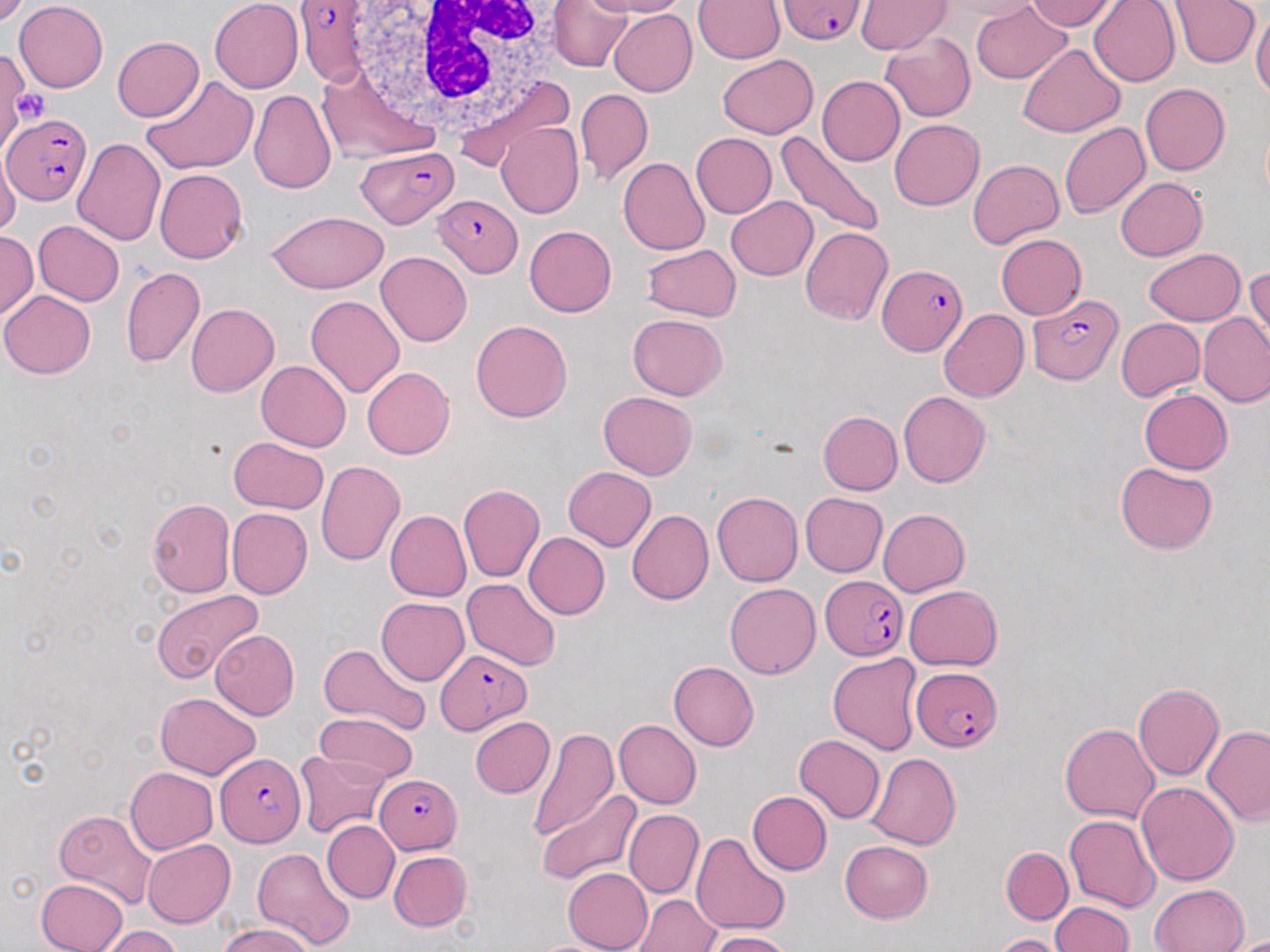

{
  "slide_level_diagnosis": "Plasmodium falciparum",
  "preparation": "thin blood smear",
  "magnification": "1000x",
  "modality": "optical microscopy",
  "image_size": "1270×952 pixels",
  "uninfected_red_blood_cell_locations": "approximate bounding boxes as [x1, y1, x2, y2] in pixels: [14, 0, 108, 91], [209, 0, 303, 93], [551, 0, 632, 71], [589, 0, 686, 17], [694, 0, 784, 64], [1023, 0, 1119, 31], [939, 1, 1039, 21], [1089, 1, 1180, 87], [1169, 1, 1260, 69], [856, 2, 953, 56], [971, 2, 1072, 83], [609, 9, 697, 96], [1251, 9, 1270, 100], [984, 11, 1107, 115], [880, 32, 976, 122], [113, 36, 203, 121], [1018, 44, 1126, 137], [0, 49, 27, 157], [717, 55, 818, 139], [141, 75, 258, 174], [817, 76, 905, 166], [1140, 83, 1230, 176], [575, 87, 653, 184], [249, 89, 336, 192], [890, 119, 984, 210], [496, 122, 583, 218], [1058, 122, 1151, 219], [776, 131, 885, 240], [691, 133, 777, 217], [72, 138, 166, 247], [0, 153, 21, 240], [618, 157, 709, 255], [969, 159, 1063, 248], [155, 169, 248, 263], [1116, 177, 1208, 261], [726, 196, 818, 280], [266, 211, 389, 292], [33, 220, 125, 306], [524, 226, 616, 317], [800, 226, 893, 326], [1, 231, 38, 320], [995, 234, 1086, 319], [642, 243, 742, 322], [1143, 248, 1246, 325], [375, 251, 471, 346], [121, 266, 206, 368], [1244, 267, 1269, 359], [1, 290, 95, 378], [305, 294, 406, 397], [186, 303, 279, 397], [938, 309, 1029, 402], [1199, 312, 1270, 408], [628, 313, 728, 401], [1115, 318, 1205, 401], [471, 320, 572, 422], [257, 360, 351, 452], [362, 367, 454, 459], [1139, 389, 1232, 474], [598, 391, 697, 481], [898, 391, 991, 487], [817, 411, 903, 495], [228, 436, 328, 513], [315, 461, 405, 565], [1114, 463, 1217, 555], [562, 467, 655, 552], [458, 485, 544, 583], [711, 492, 803, 586], [800, 492, 888, 577], [146, 498, 235, 597], [226, 507, 313, 599], [878, 508, 969, 596], [385, 510, 471, 601], [627, 510, 713, 605], [523, 532, 610, 619], [463, 578, 561, 671], [724, 582, 821, 679], [903, 585, 1003, 671], [152, 590, 264, 682], [375, 596, 470, 685], [211, 630, 299, 720], [318, 642, 430, 735], [828, 654, 924, 754], [669, 661, 759, 751], [1133, 683, 1224, 782], [156, 692, 261, 778], [315, 712, 418, 784], [470, 717, 555, 798], [614, 719, 702, 810], [1059, 724, 1159, 823], [1202, 724, 1270, 824], [527, 728, 618, 841], [794, 734, 886, 823], [295, 750, 389, 838], [867, 752, 961, 850], [125, 766, 218, 853], [1136, 782, 1238, 885], [536, 790, 642, 887], [747, 791, 832, 875], [54, 807, 158, 908], [624, 809, 703, 898], [1064, 814, 1160, 912], [322, 820, 399, 903], [691, 832, 789, 936], [143, 840, 235, 928], [839, 841, 932, 923], [1001, 847, 1073, 923], [250, 848, 356, 950], [389, 851, 473, 930], [562, 868, 652, 952], [37, 878, 128, 952], [1149, 882, 1249, 951], [632, 894, 719, 951], [1049, 902, 1133, 952], [218, 924, 315, 952], [102, 925, 183, 952], [707, 931, 792, 952], [994, 934, 1063, 952]",
  "plasmodium_falciparum_infected_red_blood_cell_locations": "approximate bounding boxes as [x1, y1, x2, y2] in pixels: [778, 0, 866, 44], [294, 2, 377, 85], [4, 115, 90, 205], [357, 145, 456, 227], [431, 195, 522, 276], [878, 263, 968, 357], [1027, 295, 1123, 385], [821, 576, 908, 661], [436, 648, 531, 734], [911, 666, 1003, 753], [215, 753, 307, 847], [377, 773, 463, 854]",
  "platelet_locations": "approximate bounding boxes as [x1, y1, x2, y2] in pixels: [11, 87, 51, 128]",
  "stain": "May-Grünwald-Giemsa",
  "white_blood_cell_locations": "approximate bounding boxes as [x1, y1, x2, y2] in pixels: [335, 0, 581, 138]",
  "field_of_view": "one of a larger specimen"
}